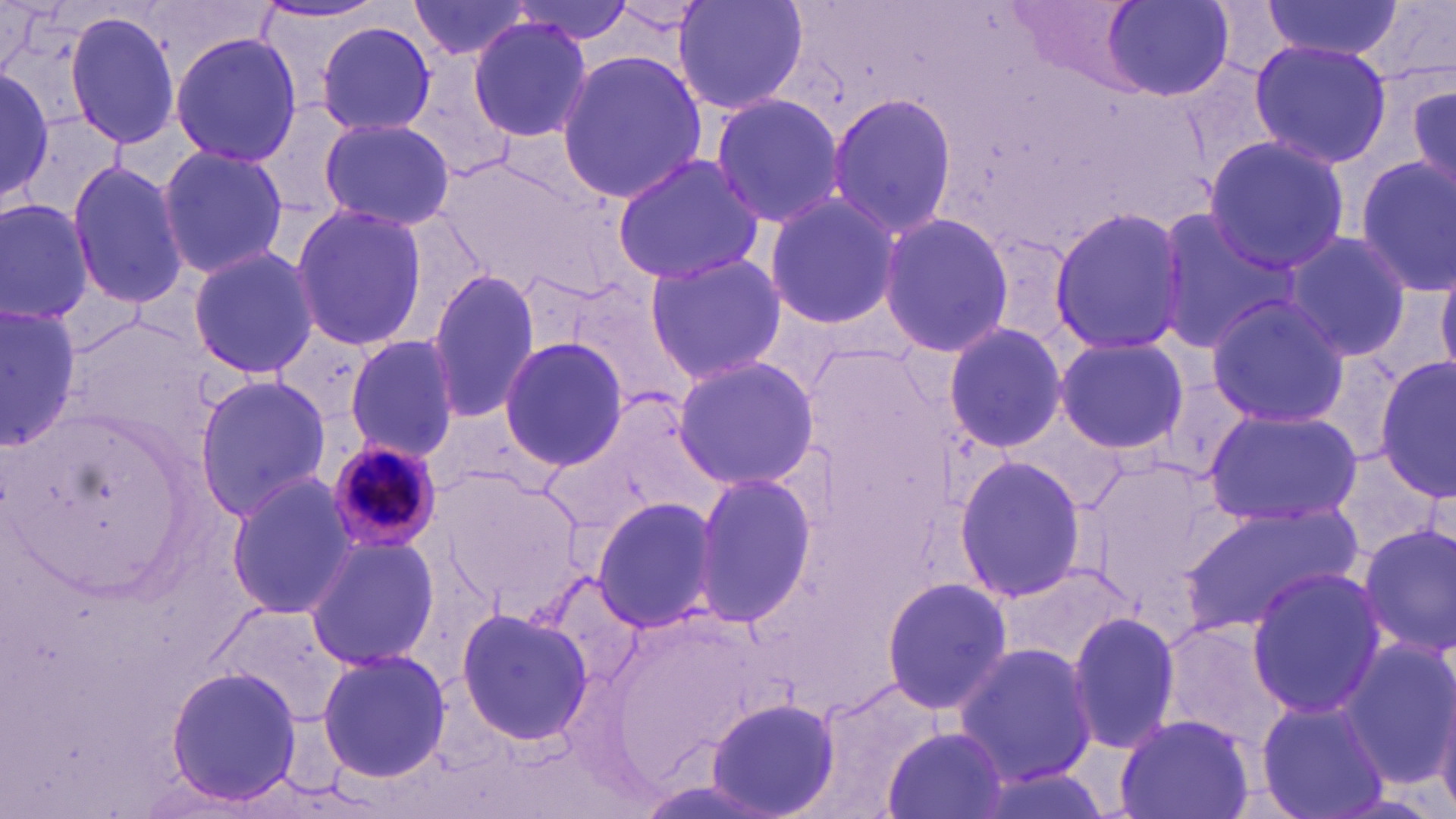

{
  "slide_level_diagnosis": "Plasmodium malariae",
  "stain": "May-Grünwald-Giemsa",
  "magnification": "1000x",
  "image_size": "1456×819 pixels",
  "modality": "light microscopy",
  "plasmodium_malariae_infected_red_blood_cell_locations": "approximate bounding boxes as named x1/y1/x2/y2 corners in pixels: (x1=324, y1=438, x2=442, y2=552)",
  "field_of_view": "one of a larger specimen",
  "preparation": "thin blood smear",
  "uninfected_red_blood_cell_locations": "approximate bounding boxes as named x1/y1/x2/y2 corners in pixels: (x1=404, y1=0, x2=542, y2=63), (x1=672, y1=0, x2=809, y2=117), (x1=1100, y1=0, x2=1235, y2=101), (x1=504, y1=1, x2=638, y2=42), (x1=1259, y1=1, x2=1401, y2=60), (x1=1361, y1=1, x2=1454, y2=100), (x1=63, y1=11, x2=181, y2=152), (x1=466, y1=15, x2=593, y2=140), (x1=317, y1=21, x2=437, y2=134), (x1=170, y1=32, x2=301, y2=168), (x1=1247, y1=40, x2=1393, y2=169), (x1=554, y1=49, x2=708, y2=205), (x1=0, y1=64, x2=52, y2=210), (x1=1404, y1=71, x2=1456, y2=203), (x1=823, y1=91, x2=957, y2=241), (x1=708, y1=93, x2=847, y2=228), (x1=317, y1=116, x2=455, y2=231), (x1=1204, y1=135, x2=1353, y2=275), (x1=154, y1=144, x2=290, y2=280), (x1=609, y1=154, x2=768, y2=286), (x1=1355, y1=158, x2=1456, y2=295), (x1=65, y1=160, x2=188, y2=311), (x1=761, y1=192, x2=898, y2=333), (x1=0, y1=196, x2=93, y2=324), (x1=289, y1=203, x2=427, y2=352), (x1=1048, y1=203, x2=1187, y2=357), (x1=1153, y1=208, x2=1298, y2=355), (x1=877, y1=211, x2=1015, y2=359), (x1=1281, y1=230, x2=1412, y2=365), (x1=188, y1=244, x2=320, y2=380), (x1=643, y1=252, x2=786, y2=385), (x1=1437, y1=265, x2=1456, y2=379), (x1=426, y1=267, x2=542, y2=424), (x1=1205, y1=296, x2=1352, y2=425), (x1=0, y1=303, x2=78, y2=450), (x1=940, y1=321, x2=1067, y2=453), (x1=344, y1=334, x2=460, y2=461), (x1=1054, y1=335, x2=1187, y2=456), (x1=498, y1=337, x2=629, y2=468), (x1=670, y1=355, x2=821, y2=491), (x1=1375, y1=357, x2=1455, y2=499), (x1=193, y1=374, x2=332, y2=519), (x1=1201, y1=407, x2=1364, y2=527), (x1=953, y1=455, x2=1088, y2=606), (x1=691, y1=471, x2=817, y2=632), (x1=226, y1=476, x2=359, y2=618), (x1=590, y1=495, x2=722, y2=634), (x1=1179, y1=504, x2=1362, y2=635), (x1=1356, y1=524, x2=1456, y2=656), (x1=302, y1=533, x2=442, y2=671), (x1=998, y1=565, x2=1138, y2=671), (x1=1244, y1=568, x2=1389, y2=720), (x1=881, y1=575, x2=1013, y2=715), (x1=454, y1=605, x2=594, y2=747), (x1=1064, y1=610, x2=1180, y2=756), (x1=1338, y1=637, x2=1455, y2=791), (x1=952, y1=642, x2=1100, y2=788), (x1=316, y1=648, x2=450, y2=784), (x1=163, y1=663, x2=303, y2=806), (x1=1428, y1=675, x2=1456, y2=819), (x1=1256, y1=695, x2=1391, y2=819), (x1=706, y1=700, x2=840, y2=818), (x1=1116, y1=713, x2=1255, y2=819), (x1=882, y1=725, x2=1010, y2=819)"
}